Locate every Plasmodium parasite.
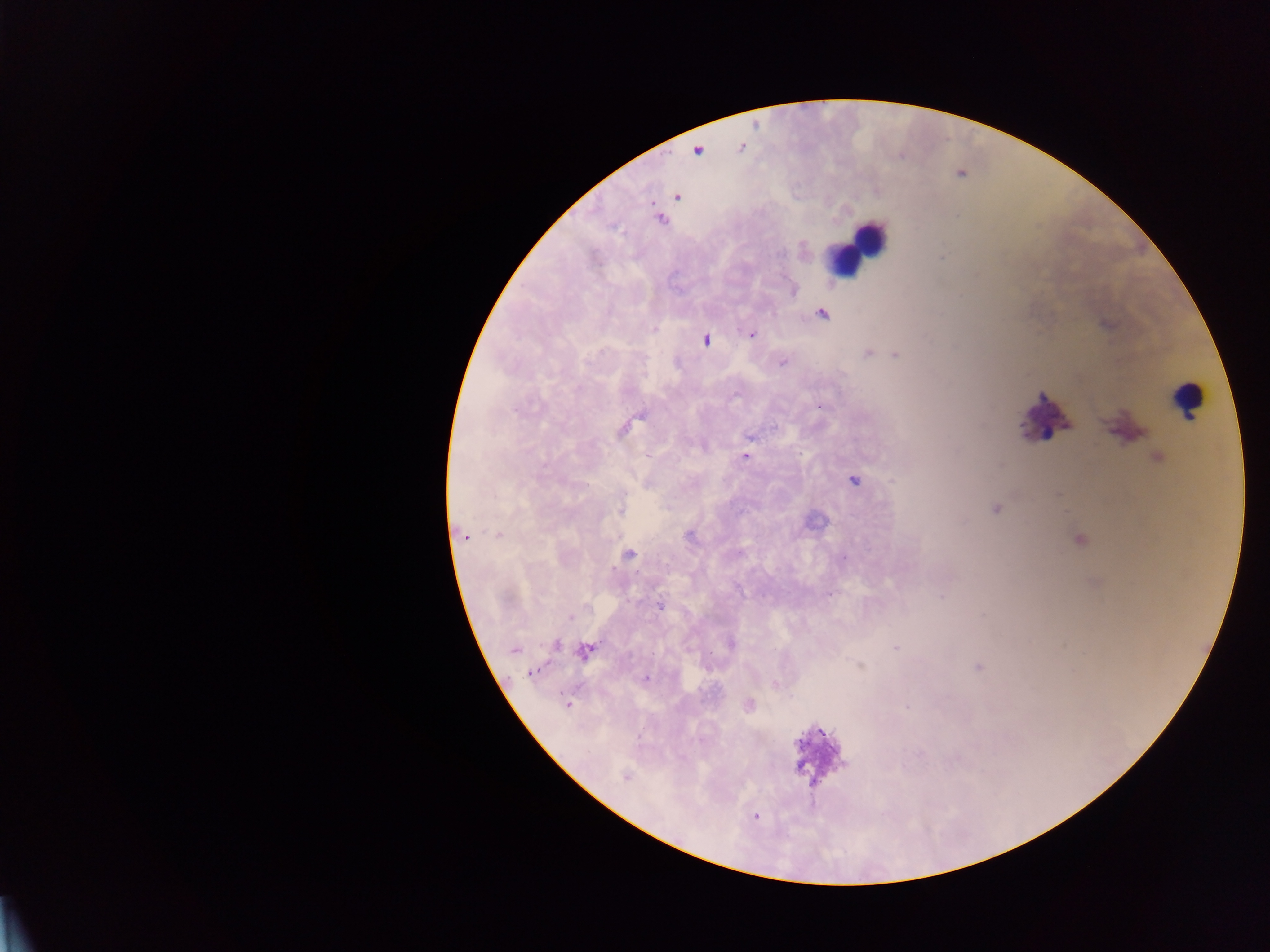

Approximate centers as {x, y} in pixels.
Plasmodium parasites: {741, 147}, {698, 150}, {677, 196}, {661, 220}, {822, 314}, {751, 334}, {705, 340}, {867, 354}, {895, 355}, {783, 363}, {820, 406}, {750, 438}, {745, 457}, {854, 481}, {996, 509}, {620, 510}, {496, 535}, {689, 535}, {465, 537}, {628, 555}, {843, 558}, {942, 597}, {660, 606}, {570, 618}, {730, 644}, {556, 645}, {895, 647}, {514, 650}, {585, 651}, {860, 666}, {978, 667}, {532, 672}, {646, 679}, {774, 684}, {568, 704}, {749, 704}, {906, 707}, {626, 777}, {755, 816}.

image size = 1270×952 pixels
field of view = single
leukocyte locations = approximate centers as {x, y} in pixels: {861, 241}, {847, 257}, {1186, 399}
country = Ghana
capture = mobile-phone photograph through a microscope
preparation = thick blood smear